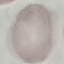
Summary:
  - Malaria status: uninfected
  - Preparation: thin smear
  - Image type: cell patch, automatically extracted from a larger field of view and resized to 64 × 64 pixels
  - Stain: Giemsa
  - Capture: smartphone through the microscope eyepiece